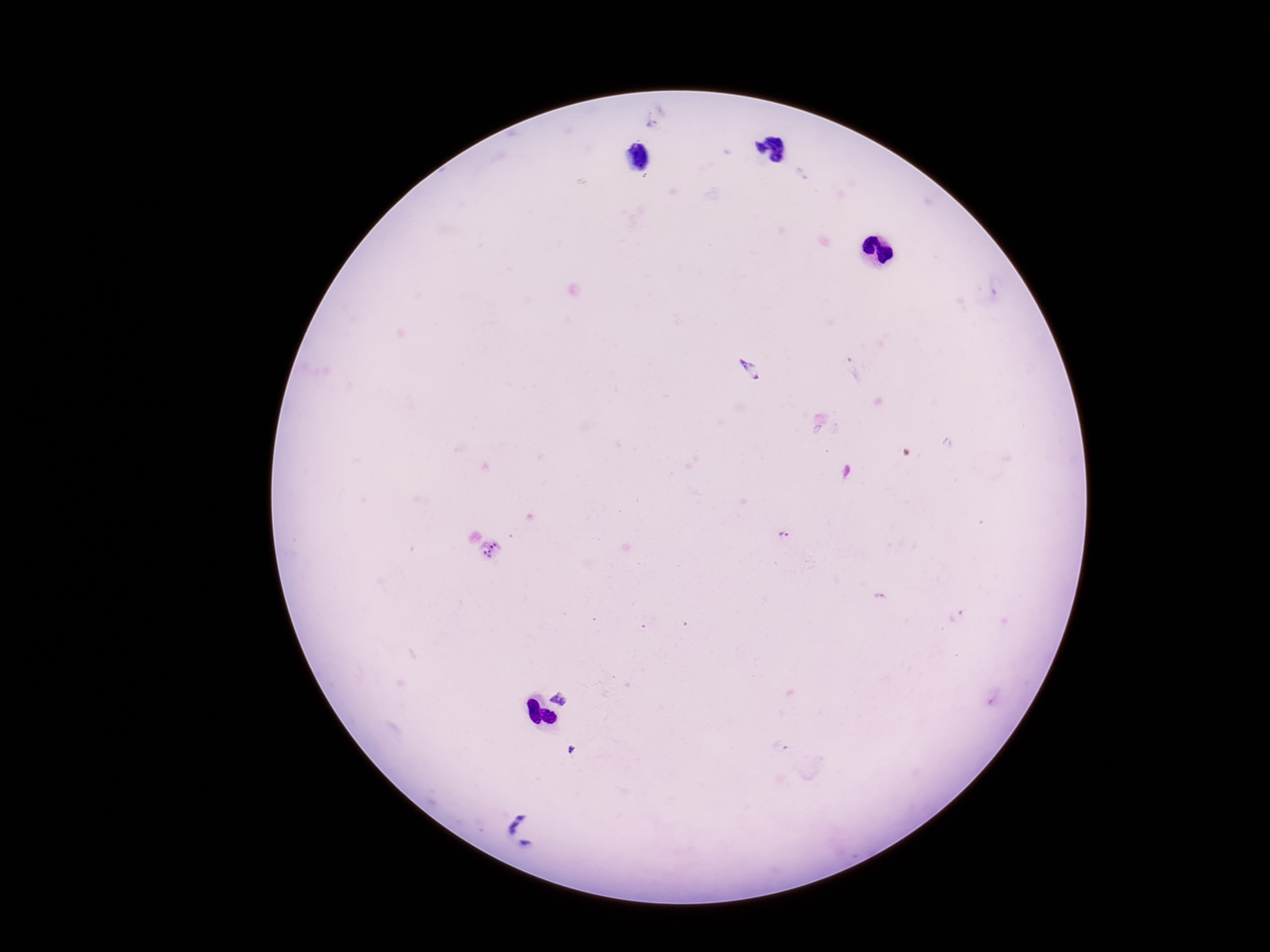

Approximate object centers, in pixels from the top-left corner.
Summary:
  - Plasmodium parasite locations: (x=652, y=124), (x=850, y=367), (x=747, y=370), (x=847, y=472), (x=785, y=535), (x=492, y=549), (x=563, y=697), (x=571, y=749), (x=521, y=815), (x=513, y=828), (x=525, y=843)
  - Field of view: one from this slide
  - Preparation: thick peripheral-blood smear
  - Capture: smartphone camera through the microscope eyepiece
  - Stain: Giemsa
  - Patient malaria status: infected
  - Magnification: 100x
  - Image size: 1270×952 pixels